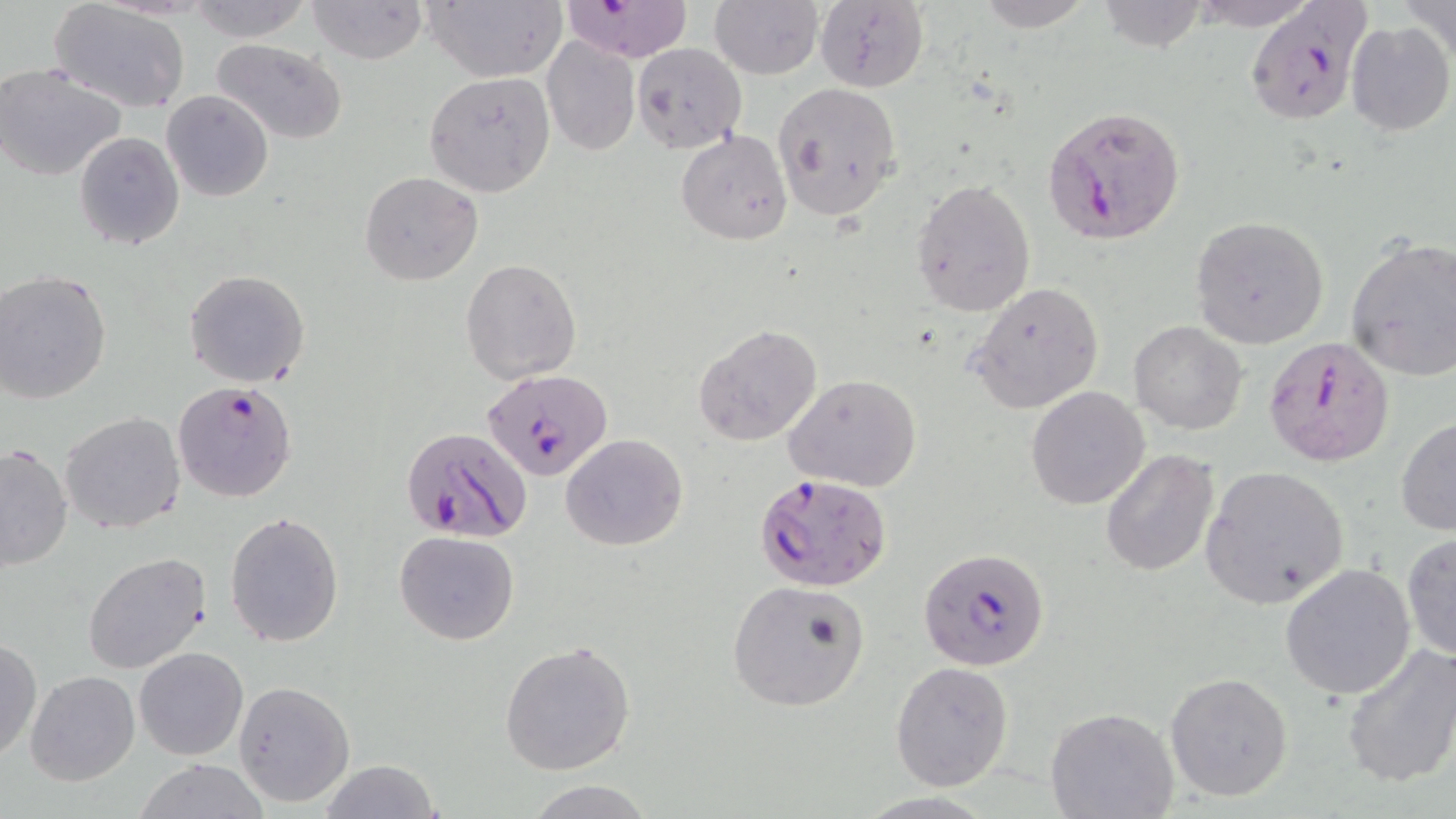 Approximate bounding boxes as (x1,y1)-(x2,y2) corner pairs in pixels. Uninfected red blood cell locations: (184,0)-(311,40), (307,0)-(428,64), (425,0)-(564,82), (709,0)-(823,78), (974,0)-(1095,30), (1399,0)-(1456,67), (559,1)-(696,61), (813,1)-(928,92), (49,2)-(191,114), (1346,22)-(1455,136), (541,35)-(639,156), (211,38)-(347,144), (631,42)-(747,153), (0,63)-(128,181), (423,71)-(555,196), (772,81)-(903,219), (161,90)-(273,202), (677,130)-(792,244), (74,132)-(184,249), (359,171)-(483,285), (912,178)-(1035,316), (1190,216)-(1329,347), (1345,237)-(1456,383), (460,258)-(582,384), (184,269)-(310,387), (0,271)-(112,403), (968,280)-(1103,414), (1129,321)-(1247,434), (693,324)-(822,445), (784,374)-(920,490), (1026,385)-(1150,511), (61,411)-(185,535), (1395,417)-(1456,536), (560,433)-(688,552), (0,441)-(74,571), (1099,448)-(1219,577), (1200,466)-(1351,608), (225,511)-(345,648), (395,531)-(519,645), (1402,534)-(1456,662), (82,552)-(212,676), (1279,564)-(1418,700), (726,581)-(869,711), (0,637)-(41,762), (500,639)-(636,777), (1340,642)-(1456,789), (134,647)-(249,761), (890,660)-(1015,792), (25,669)-(140,786), (1164,672)-(1294,801), (233,680)-(355,808), (1047,708)-(1179,819), (319,759)-(439,819), (136,760)-(265,818), (527,778)-(652,819). Plasmodium falciparum-infected red blood cell locations: (1246,0)-(1371,127), (1042,105)-(1186,244), (1262,335)-(1393,466), (484,367)-(613,482), (172,380)-(298,504), (400,430)-(529,543), (758,473)-(892,593), (919,544)-(1050,671). Slide-level diagnosis: Plasmodium falciparum. Image is 1456×819 pixels. Single field of view. Captured at 1000x magnification. Thin blood smear. Optical microscopy. May-Grünwald-Giemsa-stained preparation.